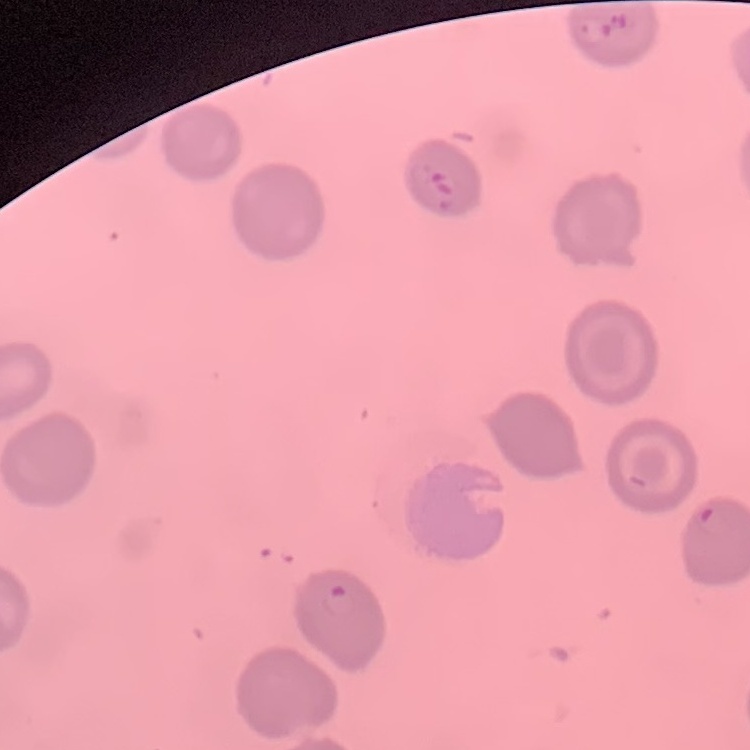
red blood cell morphology = no rouleaux formation
stain = Field's or Giemsa
image type = one tile cut from a larger photomicrograph
preparation = thin peripheral smear